Report the malaria status of this cell.
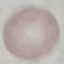

Uninfected.

Acquired by smartphone through the microscope eyepiece. Cell patch, automatically extracted from a larger field of view and resized to 64 × 64 pixels. Thin smear of blood. Giemsa stain.